Describe the morphology of the erythrocytes.
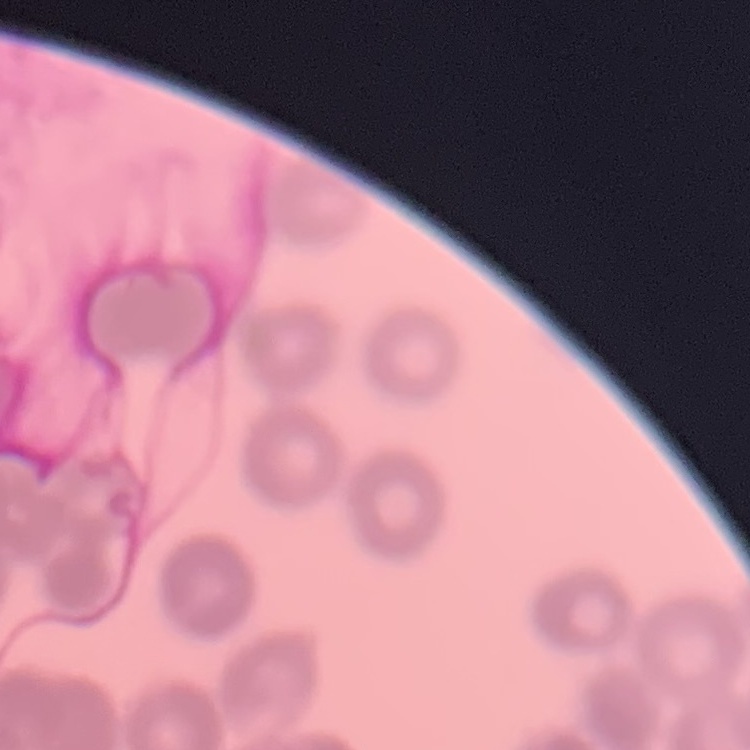

Rouleaux formation.

Thin blood film. One tile cut from a larger photomicrograph. Field's or Giemsa stain.